Outline each blood parasite and name the species.
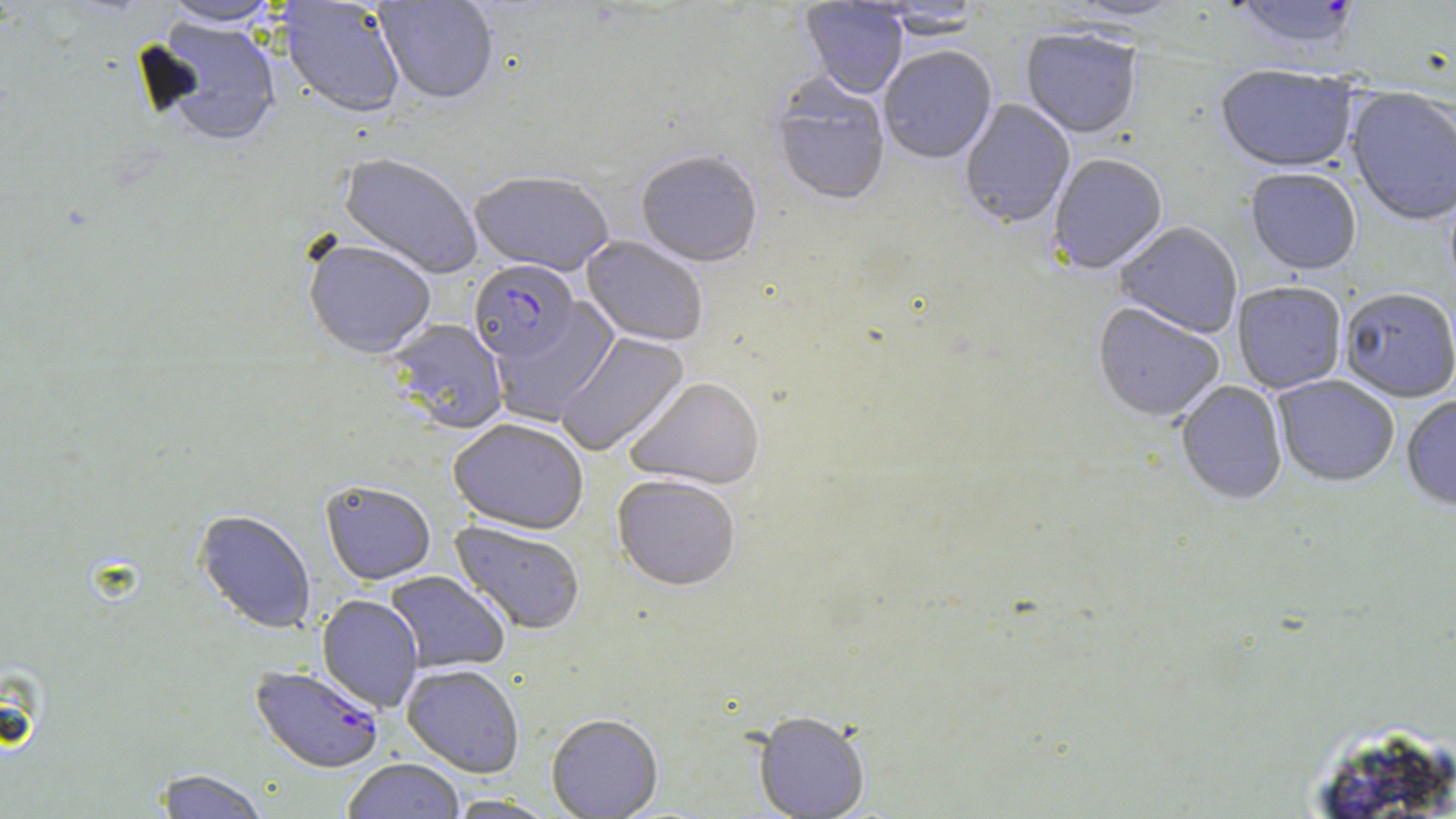
Approximate bounding boxes as [x1, y1, x2, y2] in pixels.
Plasmodium falciparum-infected red blood cells: [1227, 0, 1364, 56], [469, 261, 581, 365], [250, 665, 384, 774].
No Plasmodium ovale, Plasmodium malariae, Plasmodium vivax, Babesia divergens, or Trypanosoma brucei observed.

slide-level diagnosis = Plasmodium falciparum
uninfected red blood cell locations = approximate bounding boxes as [x1, y1, x2, y2] in pixels: [160, 0, 283, 28], [374, 0, 499, 107], [1053, 0, 1186, 25], [278, 1, 406, 120], [800, 1, 908, 100], [871, 2, 985, 41], [148, 18, 283, 148], [1021, 30, 1141, 141], [879, 48, 997, 167], [1215, 68, 1358, 175], [771, 79, 890, 208], [1345, 89, 1456, 228], [959, 100, 1075, 230], [635, 152, 762, 269], [338, 154, 482, 280], [1049, 156, 1168, 275], [1245, 171, 1361, 277], [469, 174, 614, 278], [1115, 223, 1242, 340], [581, 237, 708, 348], [303, 241, 436, 360], [1232, 283, 1347, 395], [1339, 290, 1455, 404], [490, 299, 621, 425], [1092, 304, 1225, 425], [387, 320, 508, 435], [556, 332, 691, 457], [1273, 376, 1398, 488], [625, 379, 765, 493], [1175, 381, 1287, 507], [1401, 397, 1456, 513], [448, 421, 588, 536], [611, 477, 740, 594], [321, 482, 436, 587], [193, 511, 316, 634], [449, 521, 585, 635], [385, 571, 510, 673], [317, 595, 423, 712], [401, 665, 524, 778], [753, 715, 869, 819], [546, 716, 664, 819], [342, 759, 466, 819], [152, 769, 271, 819], [446, 795, 559, 819]
preparation = thin blood smear
magnification = 1000x
stain = May-Grünwald-Giemsa
modality = light microscopy
image size = 1456×819 pixels
field of view = single